Locate every leukocyte (white blood cell).
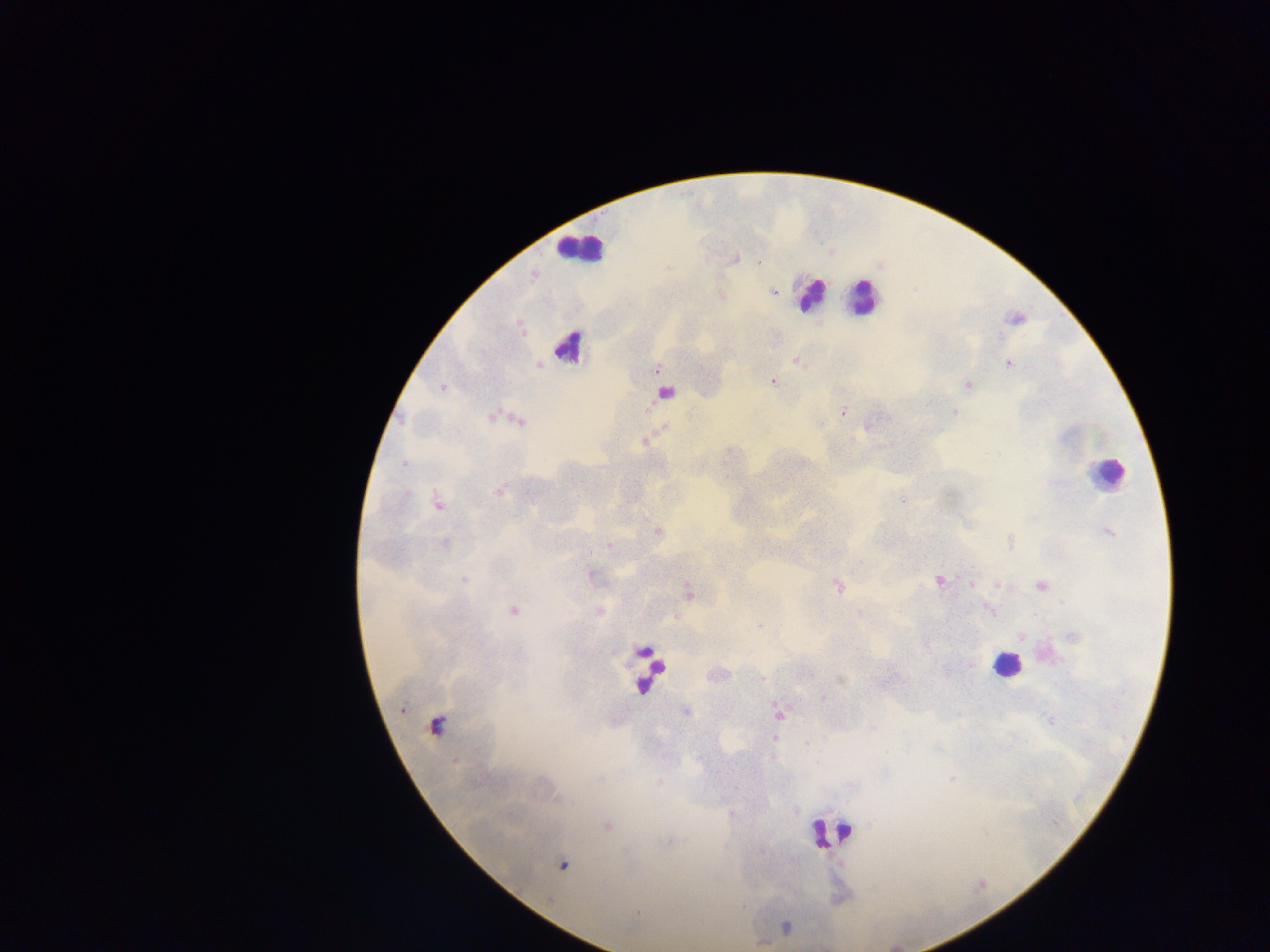

Approximate centers as {x, y} in pixels.
Leukocytes: {581, 249}, {811, 294}, {863, 297}, {567, 345}, {1108, 473}, {1005, 665}, {649, 670}, {830, 833}.

Plasmodium parasite locations: {733, 258}, {533, 275}, {773, 292}, {720, 295}, {1015, 318}, {796, 360}, {1008, 362}, {537, 364}, {656, 370}, {773, 381}, {968, 384}, {442, 386}, {665, 391}, {844, 410}, {492, 414}, {520, 420}, {870, 424}, {644, 441}, {499, 491}, {903, 501}, {438, 503}, {657, 531}, {1108, 532}, {1010, 540}, {445, 543}, {608, 545}, {591, 575}, {464, 579}, {939, 580}, {971, 584}, {997, 585}, {1041, 585}, {837, 586}, {688, 592}, {512, 610}, {990, 610}, {598, 612}, {860, 613}, {759, 626}, {1019, 636}, {1073, 636}, {762, 678}, {685, 711}, {779, 714}, {435, 725}, {873, 725}, {774, 738}, {732, 813}, {607, 827}, {563, 864}, {762, 942}. Photographed through a microscope with a mobile-phone camera. Image is 1270×952 pixels. Single field of view. Thick blood smear. Collected in Ghana.